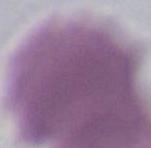

Photomicrograph. A red blood cell is seen. 1000x magnification.